State which cell type is depicted.
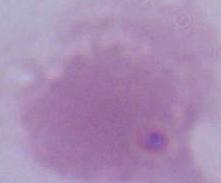

This is an erythrocyte.

magnification = 1000x
modality = photomicrograph